Classify this cell by malaria status.
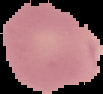
It is parasitized.

{
  "image_size": "103×94 pixels",
  "image_type": "cell region segmented out of the field of view; surrounding area masked to black",
  "preparation": "thin blood smear"
}